Assess this cell for malaria.
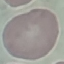
Uninfected.

stain = Giemsa
preparation = thin smear
image type = automatically extracted cell patch, resized to 64 × 64 pixels
capture = smartphone camera at the microscope eyepiece